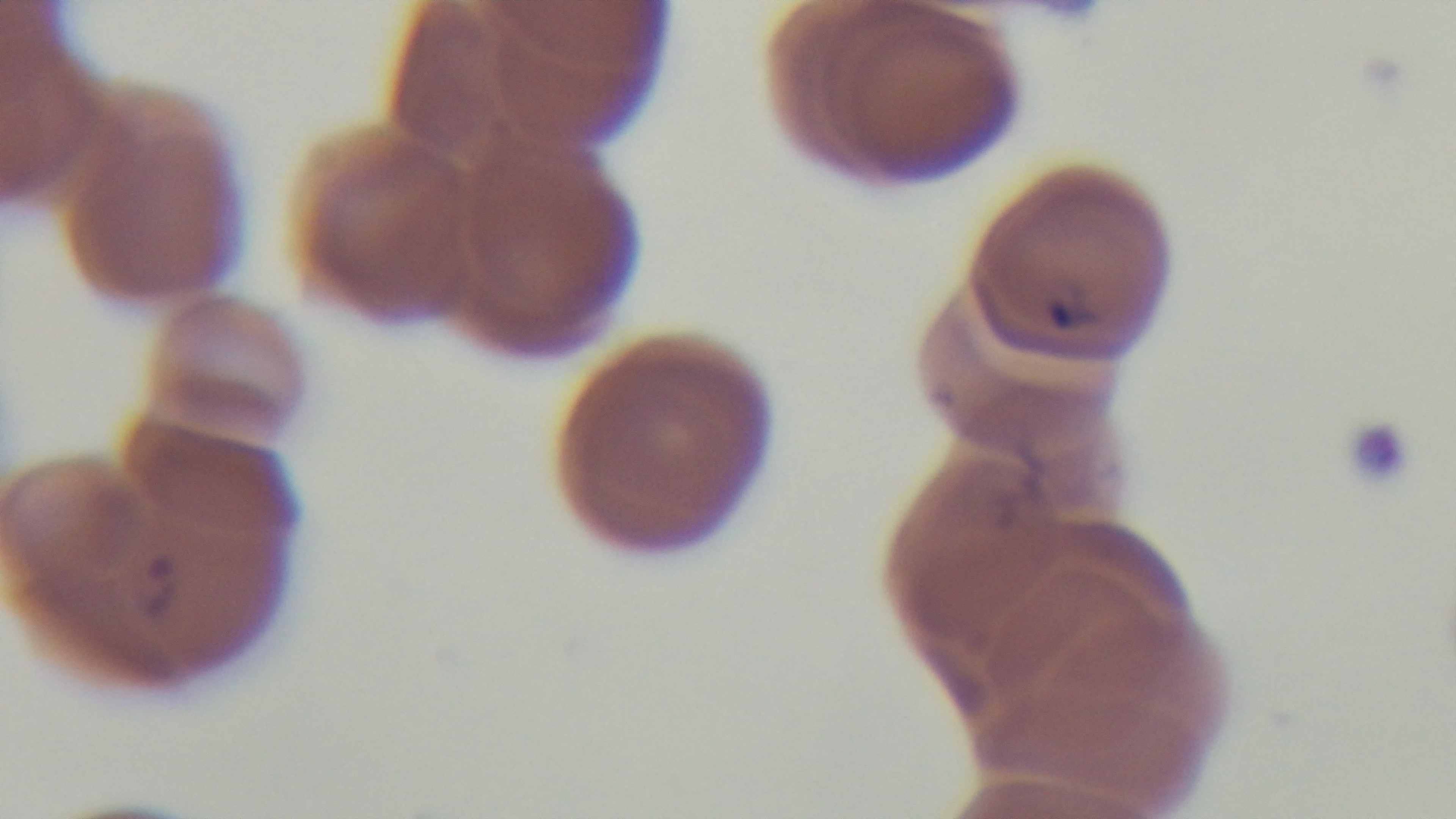
Preparation: thin. Light microscopy. Oil-immersion objective, 100x. Giemsa stain. Malaria status: positive. Mounted 4K digital camera. One field from the slide.